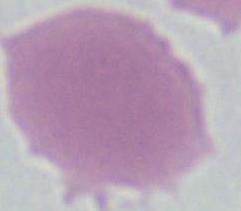

Captured at 1000x magnification. Micrograph. A red blood cell is shown.